Classify this cell by malaria status.
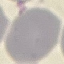

It is uninfected.

image type = cell patch, automatically extracted from a larger field of view and resized to 64 × 64 pixels
stain = Giemsa
preparation = thin blood smear
capture = smartphone through the microscope eyepiece